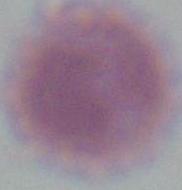
Summary:
  - Modality: photomicrograph
  - Magnification: 1000x
  - Identification: erythrocyte